Assess this cell for malaria.
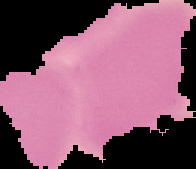

It is uninfected.

Summary:
  - Image type: cell region segmented out of the field of view; surrounding area masked to black
  - Image size: 196×169 pixels
  - Preparation: thin blood film